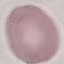

Summary:
  - Malaria status: uninfected
  - Image type: cell patch, automatically extracted from a larger field of view and resized to 64 × 64 pixels
  - Stain: Giemsa
  - Preparation: thin blood smear
  - Capture: smartphone through the microscope eyepiece